Locate every Plasmodium falciparum-infected red blood cell.
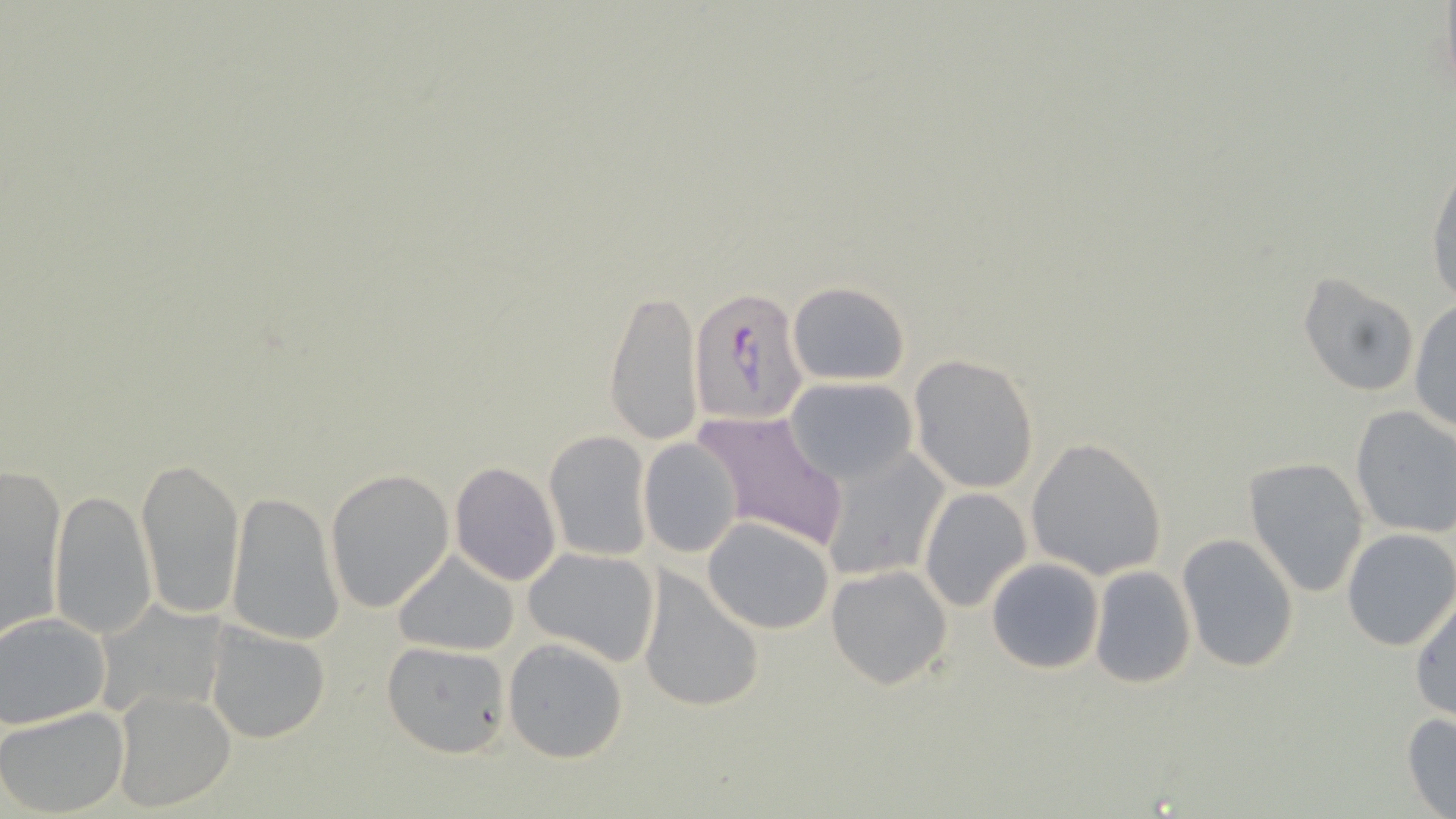

Approximate bounding boxes as [x1, y1, x2, y2] in pixels.
Plasmodium falciparum-infected red blood cells: [690, 284, 806, 428].

slide_level_diagnosis: Plasmodium falciparum
preparation: thin blood smear
magnification: 1000x
stain: May-Grünwald-Giemsa
uninfected_red_blood_cell_locations: 'approximate bounding boxes as [x1, y1, x2, y2] in pixels: [1425, 157, 1456, 307], [1299, 272, 1419, 396], [787, 281, 910, 385], [603, 286, 703, 446], [1408, 298, 1456, 436], [907, 355, 1039, 493], [784, 377, 919, 485], [1348, 405, 1456, 538], [691, 408, 849, 553], [542, 431, 653, 561], [638, 435, 744, 560], [1025, 437, 1169, 579], [818, 446, 950, 583], [137, 454, 245, 620], [1243, 457, 1369, 599], [449, 462, 561, 585], [0, 463, 68, 640], [325, 469, 455, 612], [48, 487, 155, 639], [918, 488, 1031, 612], [226, 492, 346, 644], [702, 516, 835, 635], [1342, 529, 1456, 650], [1176, 531, 1299, 672], [521, 546, 662, 665], [392, 551, 520, 656], [986, 557, 1105, 674], [826, 564, 953, 689], [638, 565, 765, 715], [1090, 565, 1196, 688], [1410, 593, 1456, 723], [100, 595, 229, 721], [1, 611, 110, 729], [206, 624, 330, 744], [503, 638, 629, 763], [380, 640, 511, 760], [111, 687, 234, 811], [0, 704, 129, 817], [1402, 711, 1456, 818]'
modality: optical microscopy
field_of_view: single
image_size: 1456×819 pixels